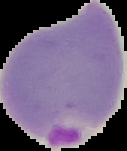
Summary:
  - Preparation: thin blood smear
  - Image size: 127×151 pixels
  - Image type: segmented cell region with the area outside set to black
  - Malaria status: parasitized